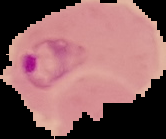

Summary:
  - Image type: segmented cell region on a black background
  - Result: Plasmodium parasites identified
  - Preparation: thin blood smear
  - Image size: 166×139 pixels